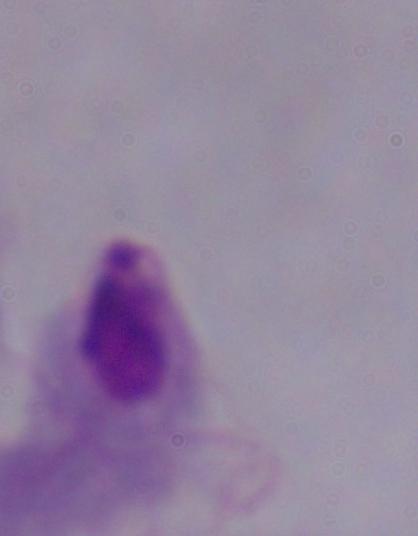

A trichomonad is shown. Captured at 1000x magnification. Micrograph.